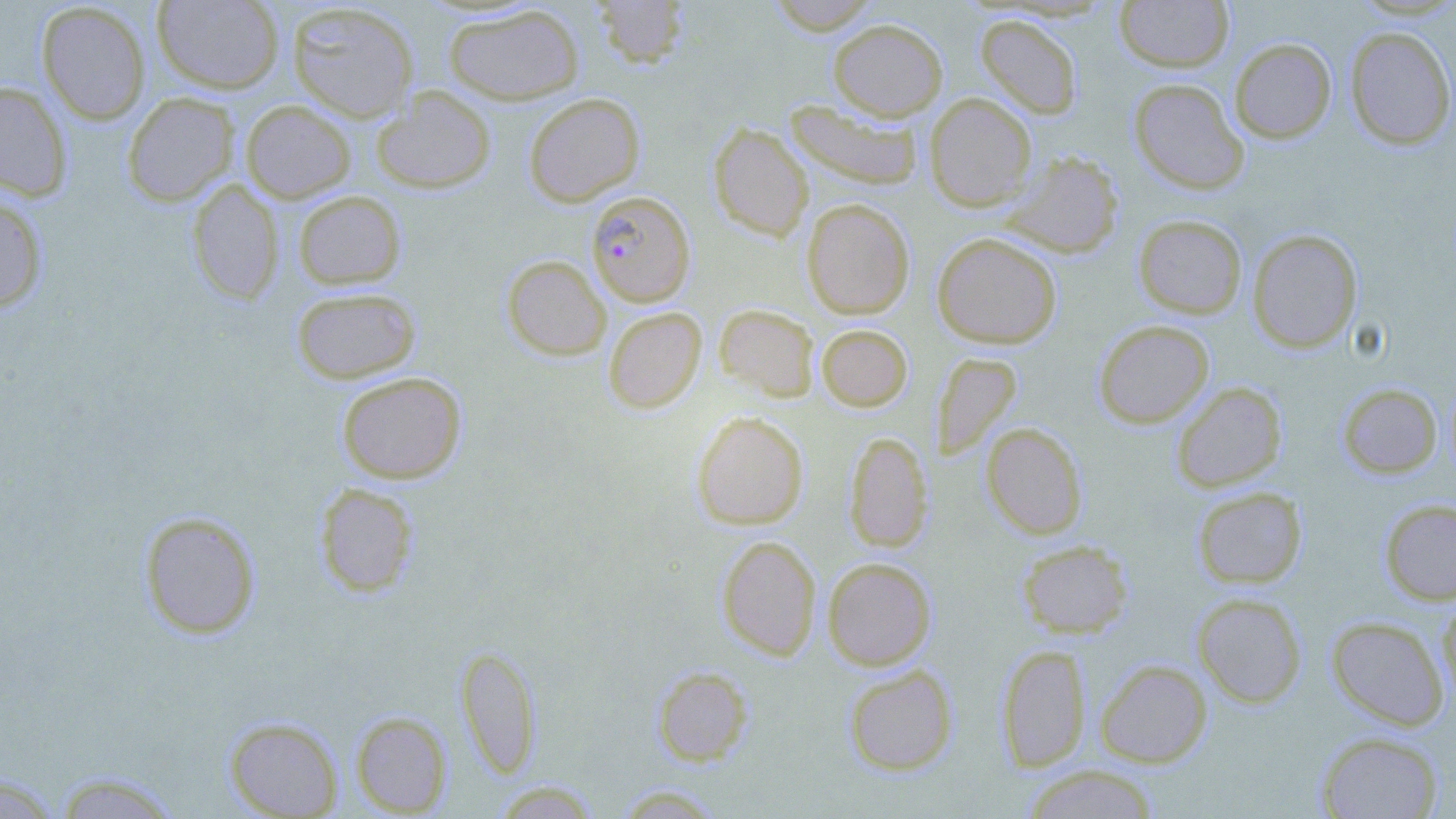 Approximate bounding boxes as [x1, y1, x2, y2] in pixels. Plasmodium falciparum-infected red blood cell locations: [586, 190, 695, 307]. Uninfected red blood cell locations: [152, 0, 285, 94], [592, 0, 690, 68], [765, 0, 882, 34], [1114, 0, 1235, 73], [36, 2, 151, 124], [287, 3, 420, 123], [442, 4, 584, 105], [975, 14, 1083, 119], [828, 18, 947, 120], [1344, 25, 1456, 151], [1229, 37, 1337, 143], [1128, 78, 1249, 195], [0, 80, 72, 201], [371, 86, 497, 194], [122, 91, 240, 206], [523, 92, 645, 207], [924, 93, 1037, 211], [240, 100, 356, 203], [784, 100, 923, 190], [708, 122, 813, 241], [1001, 150, 1124, 258], [187, 179, 284, 305], [293, 190, 407, 290], [0, 192, 49, 314], [801, 198, 915, 319], [1133, 214, 1248, 319], [1247, 229, 1363, 353], [932, 232, 1063, 349], [501, 255, 611, 361], [290, 287, 421, 384], [714, 303, 821, 402], [603, 306, 707, 415], [1093, 320, 1214, 428], [816, 324, 913, 412], [931, 351, 1022, 461], [336, 372, 467, 484], [1171, 381, 1287, 492], [1336, 382, 1442, 479], [691, 410, 809, 530], [981, 422, 1088, 539], [844, 431, 933, 552], [313, 483, 420, 597], [1192, 486, 1307, 589], [1379, 499, 1456, 605], [139, 511, 261, 639], [716, 535, 822, 660], [1016, 539, 1134, 639], [823, 557, 936, 670], [1192, 592, 1307, 708], [1437, 593, 1456, 707], [1326, 616, 1450, 730], [996, 643, 1091, 772], [455, 644, 542, 778], [1095, 659, 1212, 767], [842, 663, 958, 776], [652, 665, 753, 766], [350, 711, 453, 816], [223, 716, 344, 818], [1315, 730, 1444, 818], [1020, 764, 1161, 818], [51, 770, 184, 818], [0, 774, 63, 818], [490, 779, 602, 818], [611, 784, 728, 818]. Slide-level diagnosis: Plasmodium falciparum. Light microscopy. Thin blood smear. Single field of view. Image is 1456×819 pixels. Captured at 1000x magnification. May-Grünwald-Giemsa stain.